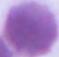
Summary:
  - Identification: red blood cell
  - Magnification: 1000x
  - Modality: micrograph